Locate every uninfected red blood cell.
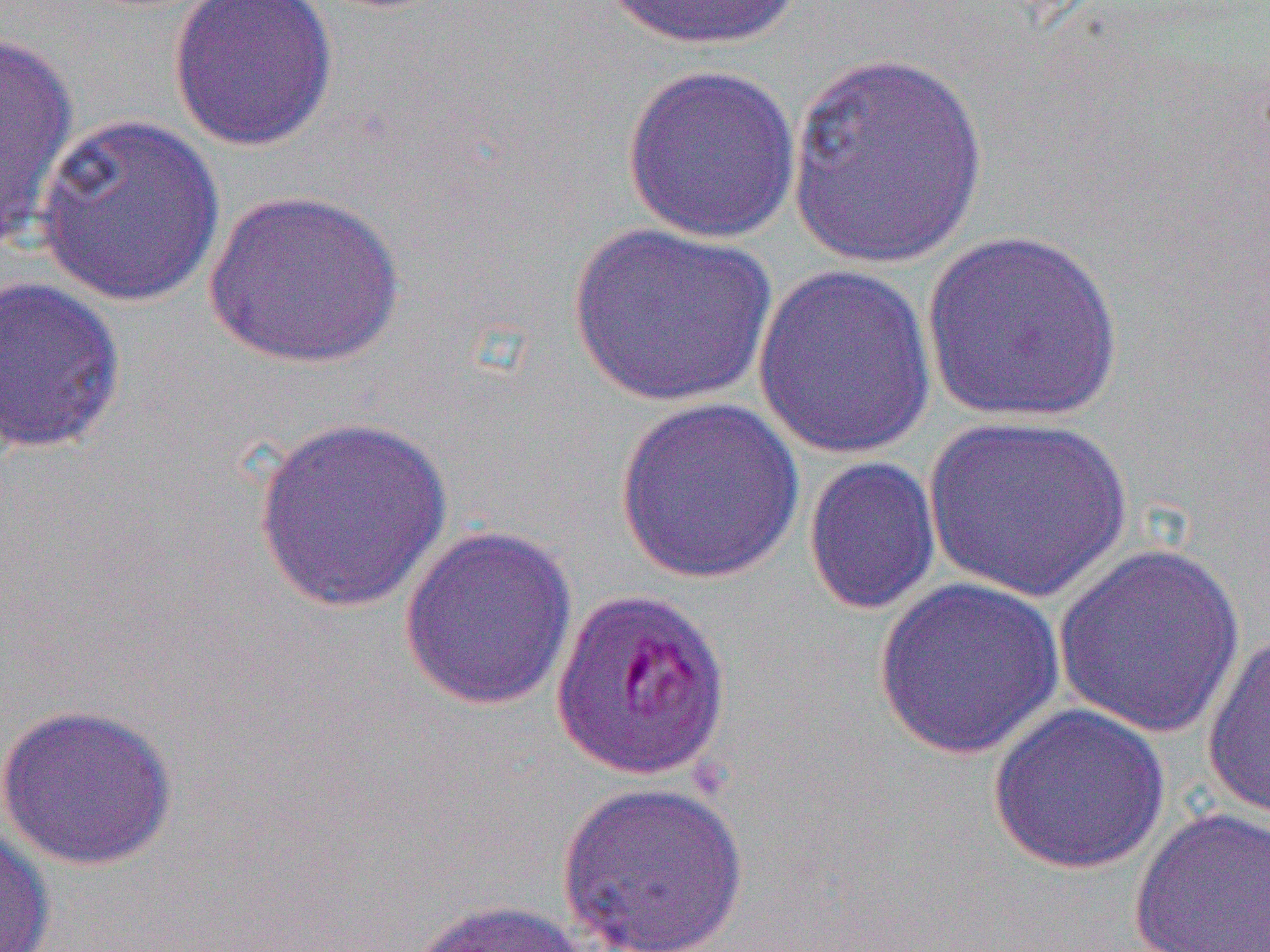

Approximate bounding boxes as (x1, y1, x2, y2) in pixels.
Uninfected red blood cells: (167, 0, 339, 152), (599, 0, 804, 51), (0, 31, 78, 250), (786, 50, 989, 269), (621, 63, 803, 244), (34, 112, 225, 307), (205, 189, 405, 370), (568, 222, 777, 410), (920, 229, 1125, 424), (752, 262, 938, 460), (0, 275, 128, 454), (614, 395, 806, 585), (921, 415, 1134, 602), (252, 416, 454, 614), (803, 455, 942, 616), (398, 524, 578, 711), (1053, 544, 1246, 740), (872, 577, 1065, 760), (1202, 632, 1270, 822), (0, 703, 178, 871), (987, 704, 1171, 874), (555, 780, 750, 952), (1129, 808, 1270, 952), (0, 824, 55, 951), (407, 898, 595, 952).

Slide-level diagnosis: Plasmodium falciparum. Optical microscopy. 1000x magnification. One field of a larger specimen. Thin blood film. Image is 1270×952 pixels.